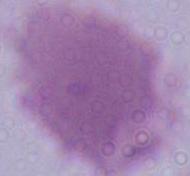
Captured at 1000x magnification. Micrograph. An erythrocyte is shown.